Name the parasite shown.
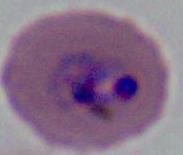
Plasmodium.

Micrograph. 400x or 1000x magnification.